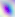

Summary:
  - Magnification: 400x
  - Identification: Toxoplasma gondii
  - Modality: micrograph